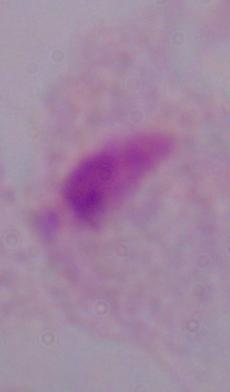
Summary:
  - Modality: photomicrograph
  - Magnification: 1000x
  - Identification: trichomonad